Report the malaria status of this cell.
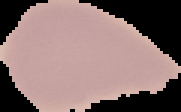
Uninfected.

Segmented cell region on a black background. Image is 181×112 pixels. From a thin blood film.